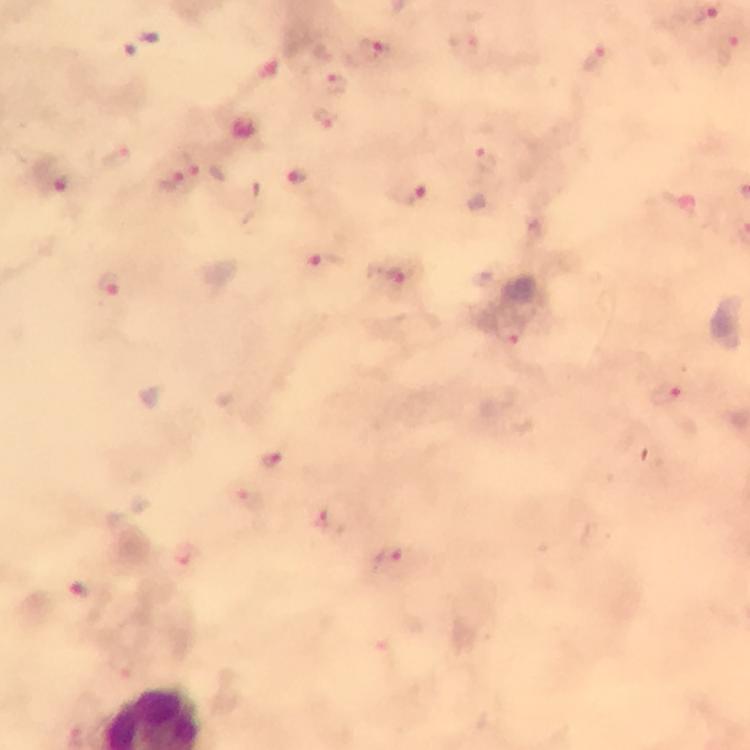
Approximate centers as {x, y} in pixels.
Summary:
  - Malaria parasite locations: {728, 47}, {375, 52}, {595, 60}, {335, 85}, {325, 117}, {491, 158}, {197, 166}, {298, 180}, {172, 185}, {66, 187}, {408, 193}, {325, 259}, {395, 277}, {111, 286}, {511, 334}, {665, 395}, {271, 460}, {324, 521}, {390, 557}, {79, 588}
  - Capture: smartphone camera through the microscope
  - Context: from a malaria diagnostic workup
  - Immersion oil: used
  - Magnification: 100x
  - Stain: Giemsa
  - Image size: 750×750 pixels
  - Cropped from: one field of view
  - Preparation: thick blood smear